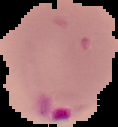

image type = cell region segmented out of the field of view; surrounding area masked to black
malaria status = parasitized
preparation = thin blood film
image size = 118×127 pixels